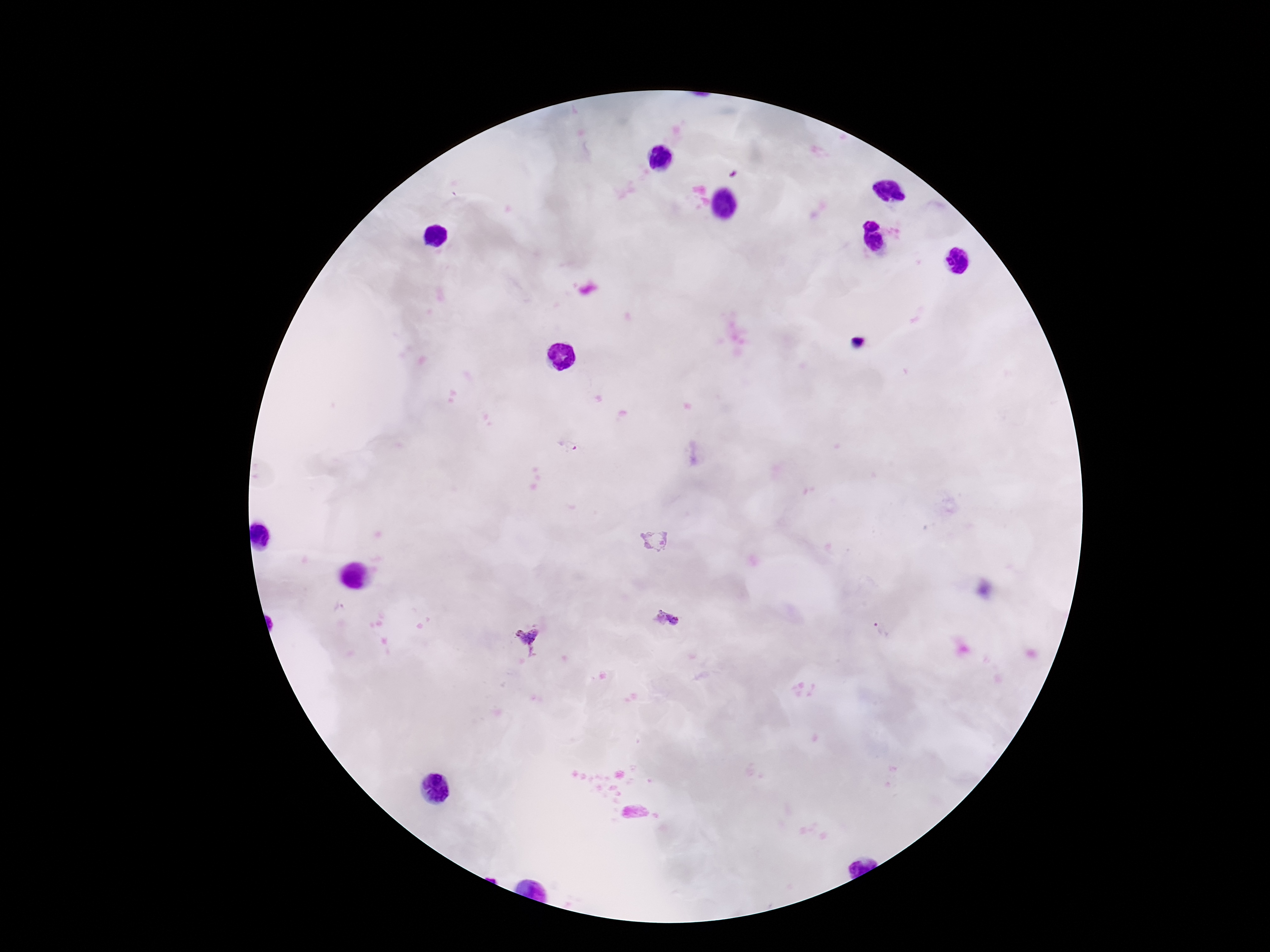

Approximate object centers, in pixels from the top-left corner.
Summary:
  - Plasmodium parasite locations: (x=568, y=445), (x=655, y=540), (x=665, y=619), (x=882, y=629), (x=526, y=640)
  - Stain: Giemsa
  - Patient malaria status: positive
  - Magnification: 100x
  - Field of view: one from this slide
  - Preparation: thick blood smear
  - Capture: smartphone camera through the microscope eyepiece
  - Image size: 1270×952 pixels